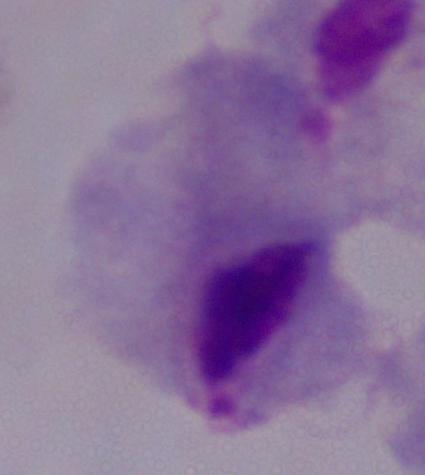
Summary:
  - Identification: trichomonad
  - Modality: micrograph
  - Magnification: 1000x